Give the position of every malaria parasite.
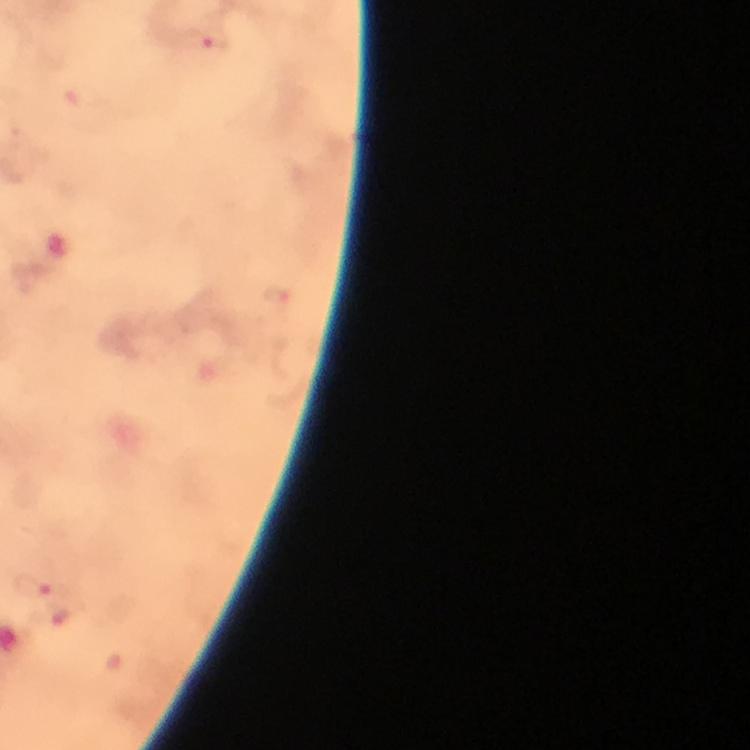

Approximate centers as {x, y} in pixels.
Malaria parasites: {210, 41}, {33, 585}.

Image is 750×750 pixels. Giemsa-stained preparation. Thick smear. A crop from one field of view. Photographed with a smartphone mounted on the microscope. 100x magnification. Immersion oil applied. From a diagnostic examination for malaria.